Locate and identify every blood parasite.
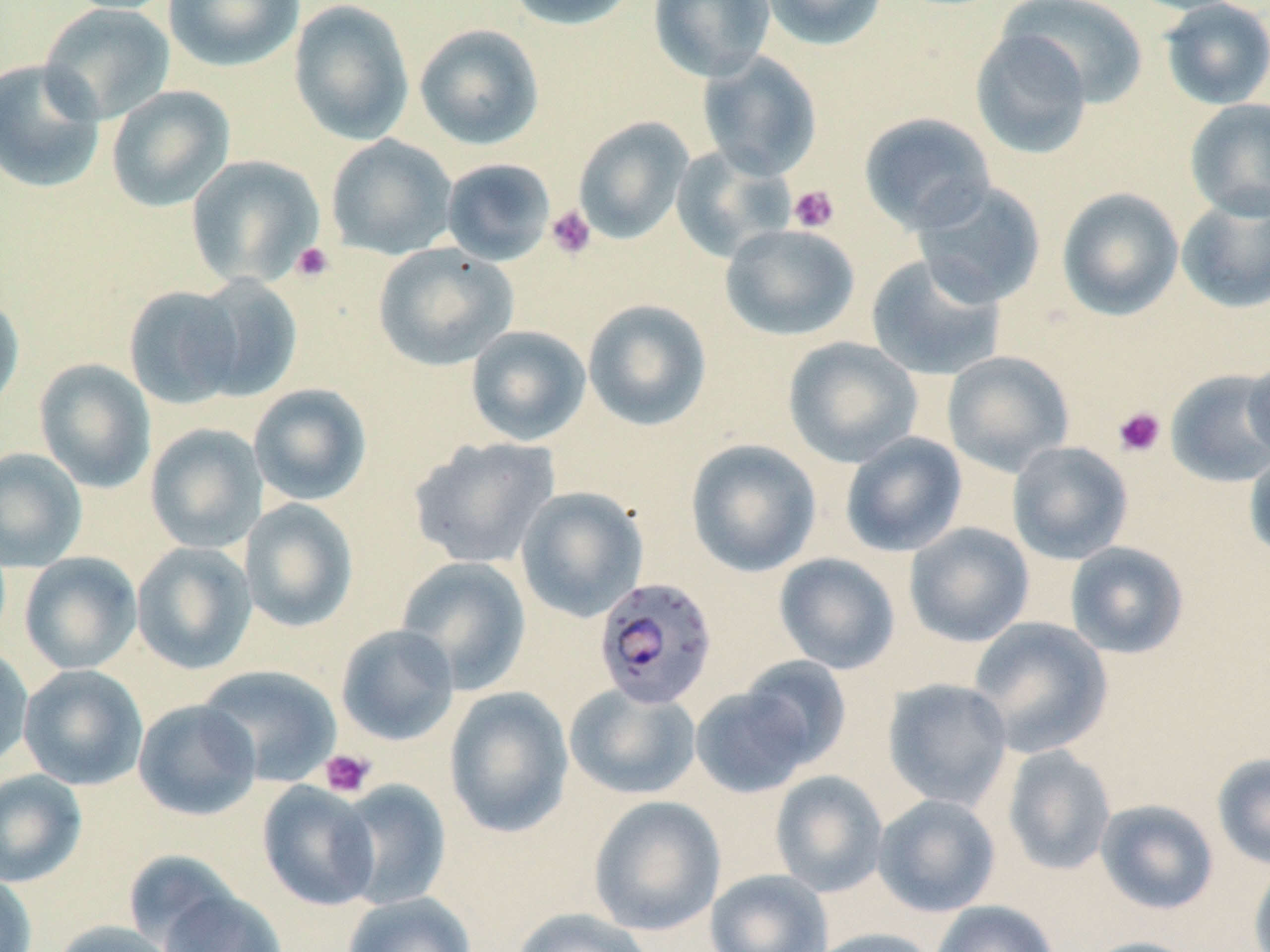
Approximate bounding boxes as (x1, y1, x2, y2) in pixels.
Plasmodium falciparum-infected red blood cells: (593, 577, 718, 710).
No Plasmodium ovale, Plasmodium malariae, Plasmodium vivax, Babesia divergens, or Trypanosoma brucei observed.

{
  "slide_level_diagnosis": "Plasmodium falciparum",
  "image_size": "1270×952 pixels",
  "preparation": "thin blood smear",
  "modality": "light microscopy",
  "stain": "May-Grünwald-Giemsa",
  "field_of_view": "single",
  "platelet_locations": "approximate bounding boxes as (x1, y1, x2, y2) in pixels: (788, 184, 840, 233), (546, 204, 597, 260), (291, 241, 335, 283), (1112, 406, 1166, 457), (319, 748, 377, 798)",
  "uninfected_red_blood_cell_locations": "approximate bounding boxes as (x1, y1, x2, y2) in pixels: (57, 0, 181, 15), (163, 0, 305, 72), (505, 0, 640, 30), (649, 0, 776, 81), (759, 0, 890, 50), (1121, 0, 1252, 15), (288, 1, 415, 145), (999, 1, 1149, 107), (1159, 1, 1270, 110), (38, 3, 176, 125), (414, 23, 545, 151), (970, 28, 1093, 159), (697, 51, 823, 180), (0, 58, 106, 195), (106, 84, 235, 212), (1185, 98, 1270, 221), (858, 112, 997, 234), (573, 116, 694, 244), (325, 134, 457, 260), (671, 145, 796, 262), (185, 154, 325, 289), (441, 158, 556, 266), (912, 180, 1047, 307), (1057, 187, 1184, 320), (1176, 192, 1270, 314), (720, 224, 860, 341), (373, 242, 519, 371), (866, 253, 1007, 381), (188, 274, 304, 402), (123, 285, 245, 409), (0, 293, 25, 418), (582, 298, 713, 431), (465, 325, 591, 446), (783, 336, 923, 468), (942, 351, 1075, 476), (1243, 352, 1270, 466), (34, 358, 156, 493), (1165, 368, 1270, 487), (248, 384, 371, 506), (144, 423, 268, 553), (839, 432, 968, 557), (408, 436, 560, 569), (685, 439, 821, 577), (1007, 441, 1133, 565), (0, 447, 87, 572), (1244, 451, 1270, 563), (515, 486, 648, 622), (239, 498, 359, 633), (904, 522, 1034, 647), (131, 541, 258, 674), (1065, 541, 1189, 659), (19, 552, 142, 674), (773, 553, 900, 674), (395, 555, 531, 694), (968, 617, 1112, 758), (335, 624, 459, 746), (0, 643, 34, 771), (736, 656, 852, 770), (18, 664, 148, 790), (197, 664, 342, 787), (882, 678, 1013, 810), (565, 683, 701, 800), (690, 683, 819, 798), (444, 686, 574, 838), (133, 699, 261, 820), (1002, 745, 1116, 876), (1212, 752, 1270, 870), (0, 769, 88, 888), (770, 770, 888, 897), (334, 779, 452, 910), (256, 781, 381, 911), (872, 794, 1000, 917), (588, 795, 726, 936), (1095, 799, 1219, 915), (1249, 859, 1270, 952), (705, 869, 832, 952), (0, 871, 38, 952), (156, 886, 288, 952), (342, 892, 477, 952), (930, 900, 1060, 952), (511, 907, 656, 952), (51, 920, 180, 952), (808, 927, 941, 952), (1079, 936, 1204, 952)",
  "magnification": "1000x"
}